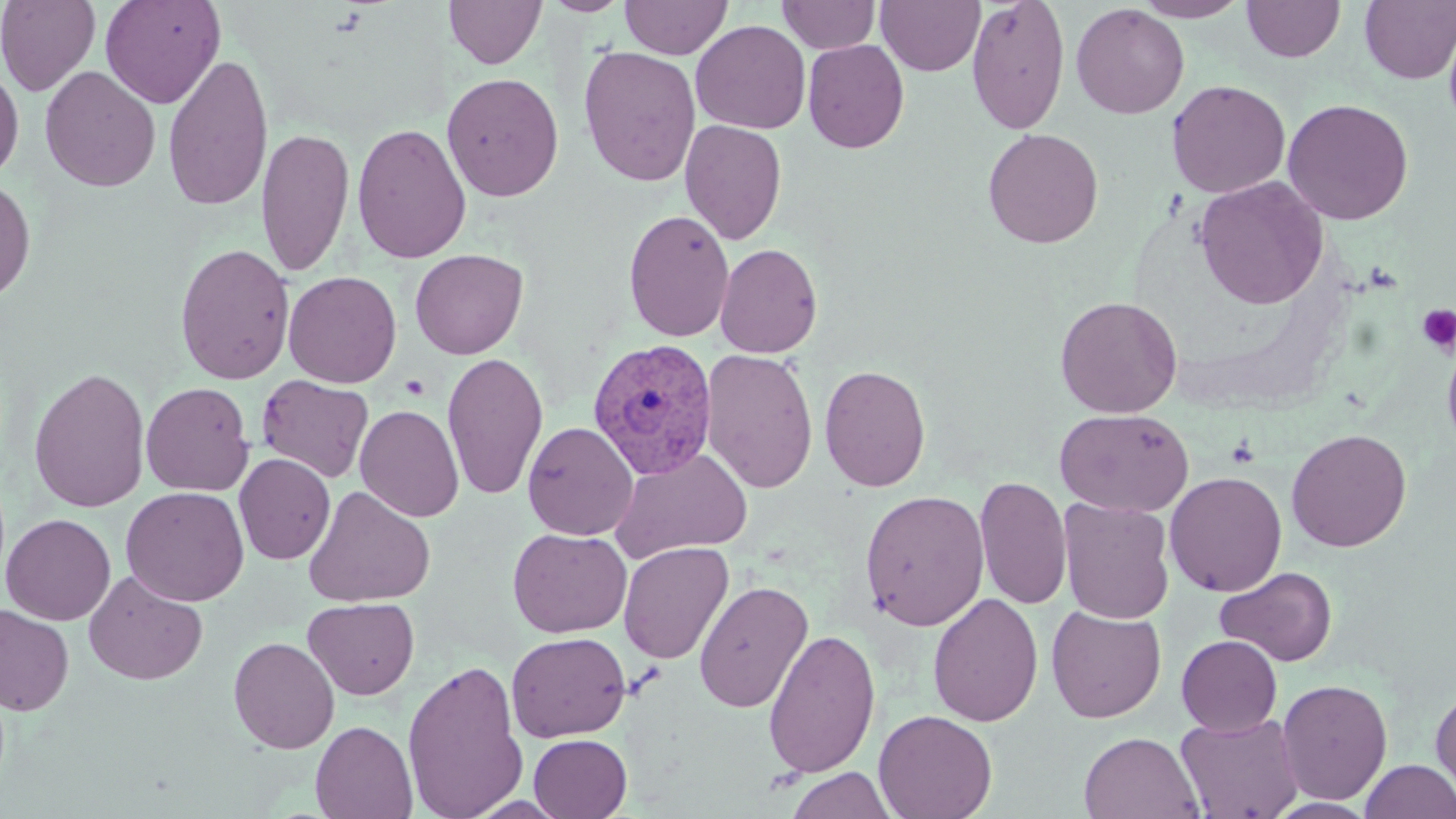
Summary:
  - Coordinate format: approximate bounding boxes as [x1, y1, x2, y2] in pixels
  - Plasmodium vivax-infected red blood cell locations: [587, 337, 719, 479]
  - Uninfected red blood cell locations: [1, 0, 100, 95], [100, 0, 225, 109], [543, 0, 632, 16], [620, 0, 732, 59], [777, 0, 880, 54], [876, 0, 985, 76], [966, 0, 1071, 134], [1133, 0, 1250, 22], [444, 1, 547, 69], [1242, 1, 1345, 63], [1359, 1, 1456, 85], [1071, 3, 1189, 119], [690, 19, 811, 134], [802, 39, 909, 154], [578, 45, 701, 187], [162, 51, 274, 212], [0, 62, 25, 184], [39, 65, 161, 192], [442, 72, 564, 202], [1167, 80, 1291, 198], [1282, 98, 1414, 225], [680, 119, 787, 245], [352, 122, 471, 265], [257, 126, 355, 277], [982, 127, 1104, 249], [0, 175, 37, 304], [1194, 177, 1329, 309], [623, 209, 735, 343], [715, 242, 823, 358], [174, 243, 295, 385], [409, 249, 528, 359], [282, 270, 402, 388], [1055, 296, 1183, 417], [1441, 330, 1456, 459], [700, 348, 819, 494], [442, 352, 549, 501], [819, 364, 930, 492], [28, 366, 150, 513], [256, 375, 374, 483], [140, 381, 254, 496], [355, 404, 464, 522], [1054, 408, 1194, 517], [522, 421, 638, 540], [1286, 428, 1412, 552], [610, 447, 753, 562], [234, 453, 335, 565], [234, 462, 423, 589], [1164, 471, 1288, 597], [975, 475, 1073, 610], [120, 486, 249, 607], [303, 486, 436, 607], [859, 489, 990, 631], [1057, 497, 1175, 624], [1, 513, 116, 625], [508, 527, 632, 638], [618, 541, 735, 665], [1216, 566, 1337, 666], [83, 568, 207, 686], [694, 579, 813, 714], [928, 593, 1044, 727], [303, 597, 420, 700], [0, 604, 74, 716], [1046, 605, 1166, 723], [764, 627, 881, 778], [506, 631, 631, 742], [1176, 635, 1282, 736], [228, 636, 340, 754], [402, 658, 527, 819], [1276, 678, 1393, 805], [1431, 682, 1456, 806], [873, 709, 997, 819], [1175, 712, 1304, 819], [311, 720, 417, 819], [1079, 732, 1204, 818], [528, 733, 632, 818], [1359, 759, 1456, 819], [786, 768, 897, 819]
  - Platelet locations: [1416, 304, 1456, 354]
  - Slide-level diagnosis: Plasmodium vivax
  - Modality: optical microscopy
  - Preparation: thin blood smear
  - Field of view: single
  - Magnification: 1000x
  - Stain: May-Grünwald-Giemsa
  - Image size: 1456×819 pixels